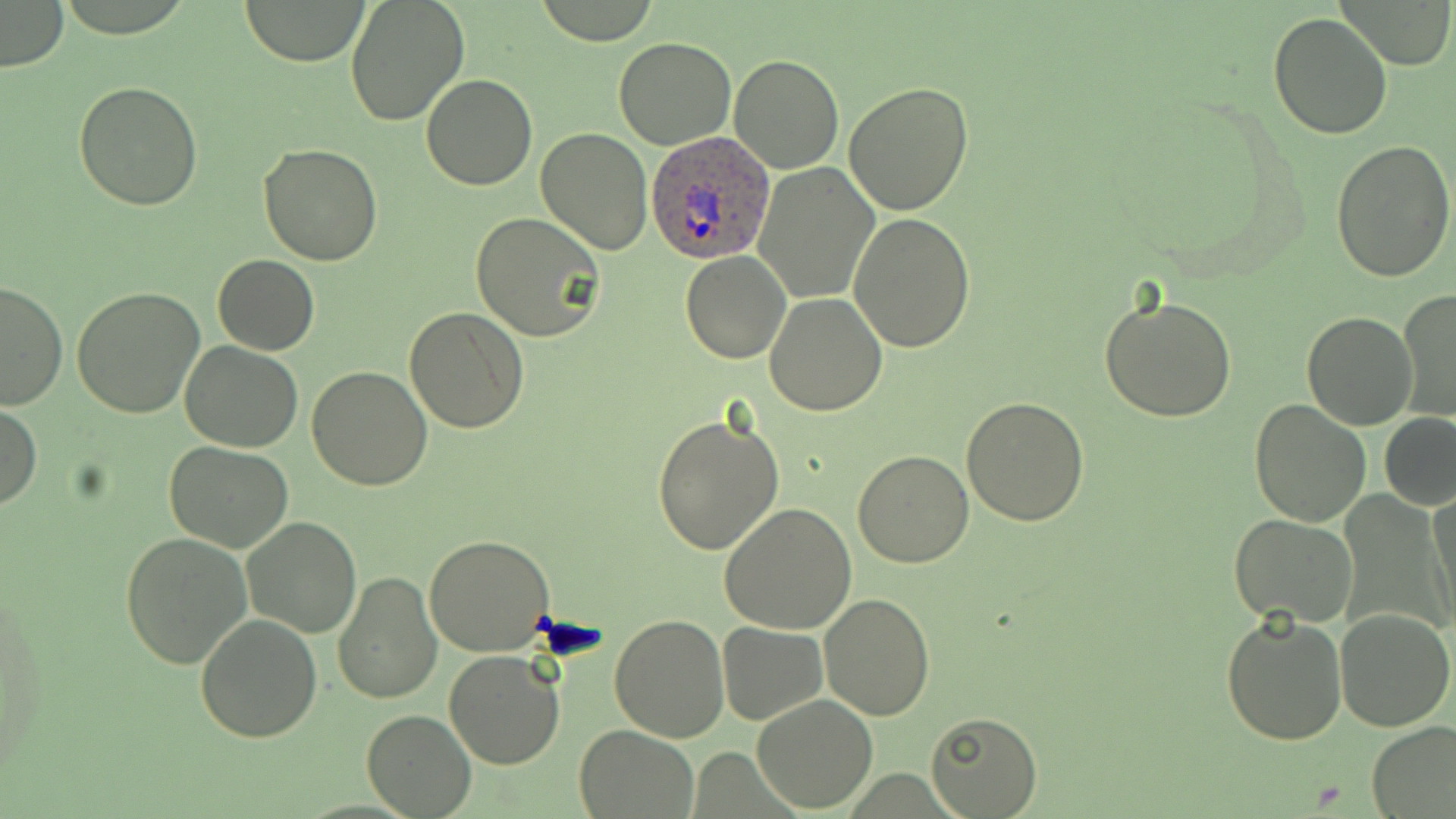
Summary:
  - Coordinate format: approximate bounding boxes as [x1, y1, x2, y2] in pixels
  - Plasmodium ovale-infected red blood cell locations: [647, 132, 776, 263]
  - Platelet locations: [539, 616, 608, 663]
  - Uninfected red blood cell locations: [240, 0, 369, 66], [346, 0, 471, 125], [530, 1, 662, 44], [1, 2, 68, 72], [1267, 11, 1395, 141], [613, 37, 738, 151], [730, 55, 843, 174], [421, 73, 537, 190], [74, 80, 203, 212], [842, 82, 974, 216], [536, 128, 653, 255], [1331, 140, 1456, 286], [258, 143, 383, 265], [755, 165, 878, 303], [470, 211, 606, 342], [848, 212, 976, 353], [680, 250, 791, 363], [213, 255, 319, 356], [1, 280, 67, 411], [72, 284, 204, 418], [1398, 289, 1455, 422], [765, 291, 888, 415], [1101, 294, 1238, 423], [404, 305, 529, 433], [1301, 309, 1418, 429], [180, 342, 302, 452], [307, 366, 432, 491], [961, 395, 1089, 525], [1248, 400, 1371, 528], [1, 403, 42, 508], [1379, 412, 1456, 511], [652, 415, 784, 557], [164, 439, 293, 551], [852, 450, 975, 568], [1427, 488, 1456, 632], [720, 502, 858, 634], [1229, 514, 1359, 626], [241, 517, 361, 638], [120, 530, 252, 669], [425, 533, 556, 658], [333, 569, 443, 704], [821, 593, 935, 720], [1335, 608, 1454, 732], [1222, 610, 1348, 744], [609, 613, 730, 742], [195, 614, 323, 742], [716, 622, 827, 725], [443, 648, 565, 769], [751, 693, 877, 811], [361, 710, 477, 817], [924, 711, 1042, 817], [1366, 722, 1456, 818], [575, 725, 696, 818]
  - Slide-level diagnosis: Plasmodium ovale
  - Image size: 1456×819 pixels
  - Field of view: one of a larger specimen
  - Preparation: thin blood film
  - Magnification: 1000x
  - Stain: May-Grünwald-Giemsa
  - Modality: light microscopy